Identify the parasite.
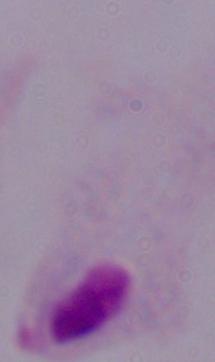
This is a trichomonad.

1000x magnification. Photomicrograph.